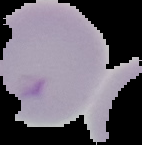
image_type: segmented cell region with the area outside set to black
preparation: thin blood film
image_size: 142×145 pixels
result: no Plasmodium parasites seen